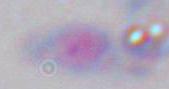

Summary:
  - Identification: Toxoplasma gondii
  - Modality: micrograph
  - Magnification: 1000x